Report the malaria status of this cell.
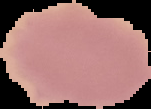

It is uninfected.

image size = 151×109 pixels
image type = segmented cell region with the area outside set to black
preparation = thin blood smear